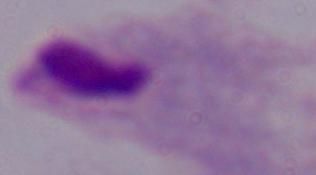

identification: trichomonad
modality: photomicrograph
magnification: 1000x